Give the preparation type.
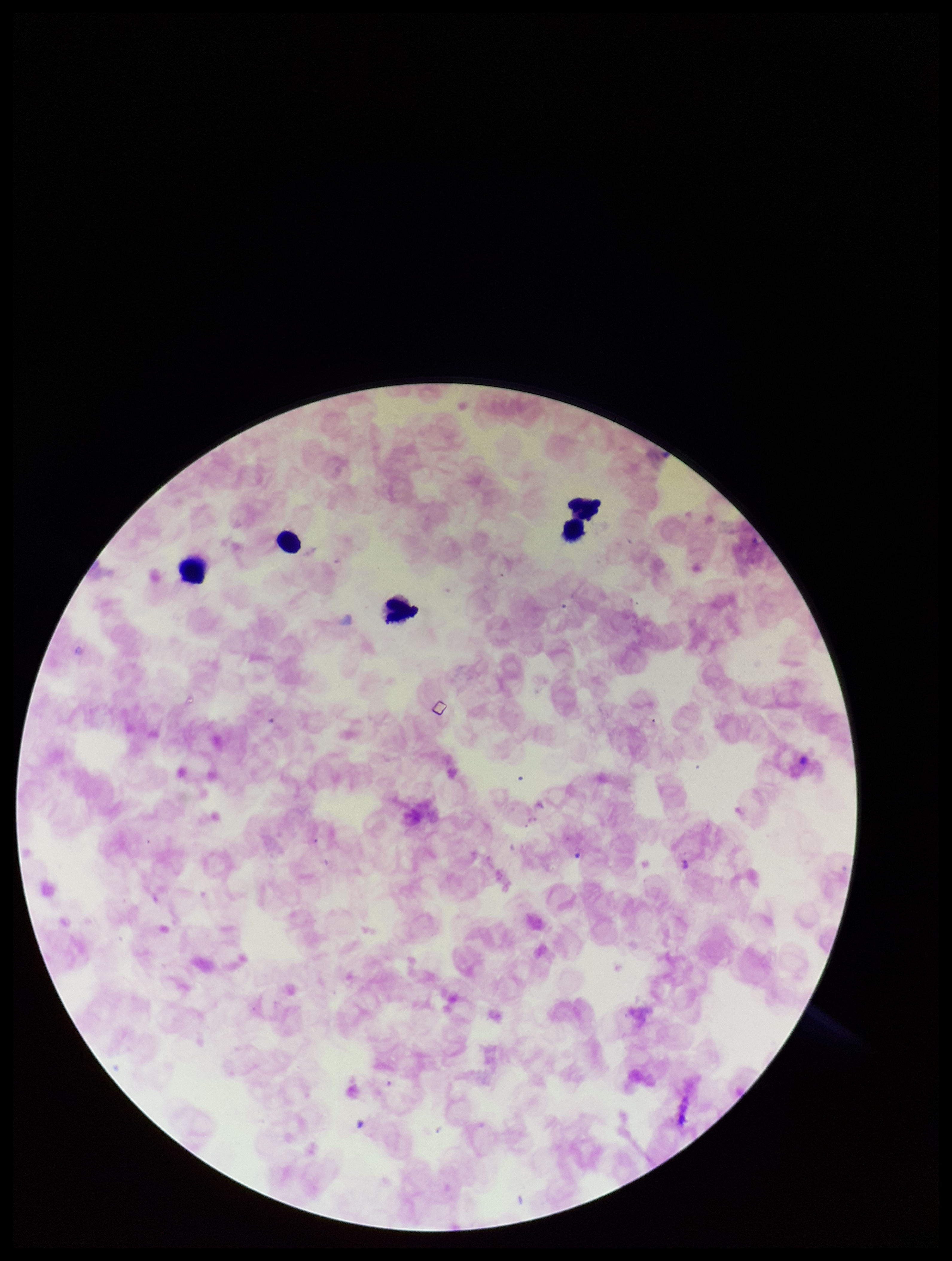
It is a thick blood smear.

Image is 952×1261 pixels. Stained with Giemsa. Plasmodium parasites: none identified. Parasite count: 0. Photographed through the microscope eyepiece with a smartphone camera. Leukocyte count: 5. Species reported for this patient: Plasmodium falciparum. Patient malaria status: infected. One field from this slide.